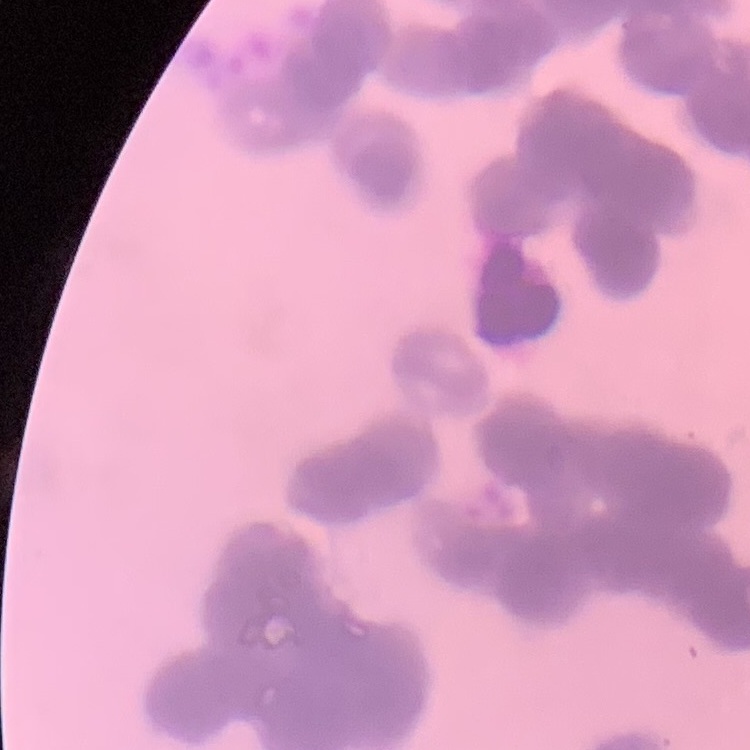

Summary:
  - Red blood cell morphology: rouleaux formation
  - Stain: Field's or Giemsa
  - Image type: square crop of a larger photomicrograph
  - Preparation: thin blood film